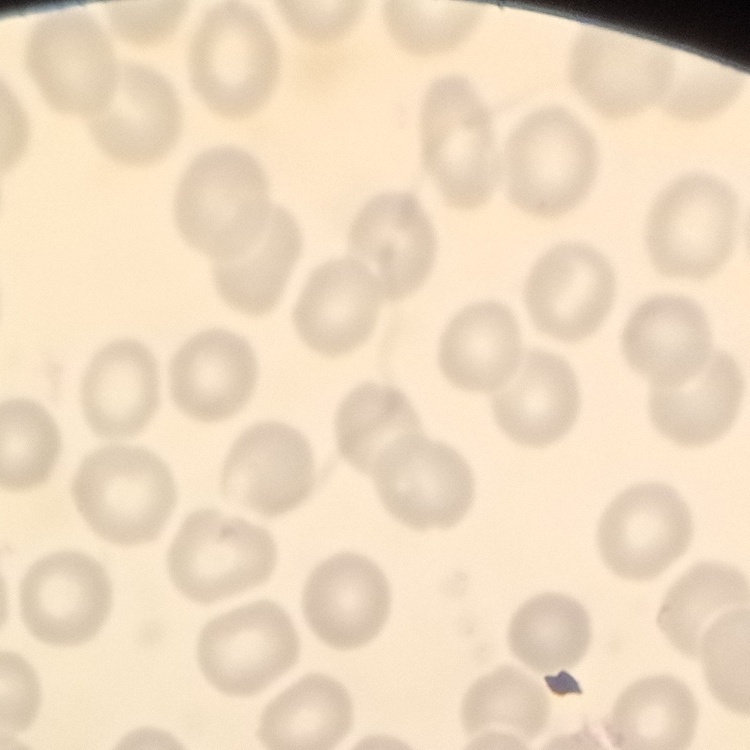
erythrocyte morphology = no rouleaux formation
stain = Field's or Giemsa
preparation = thin blood film
image type = one tile cut from a larger photomicrograph